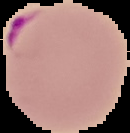
image size = 130×133 pixels
malaria status = parasitized
image type = segmented cell region on a black background
preparation = thin blood film